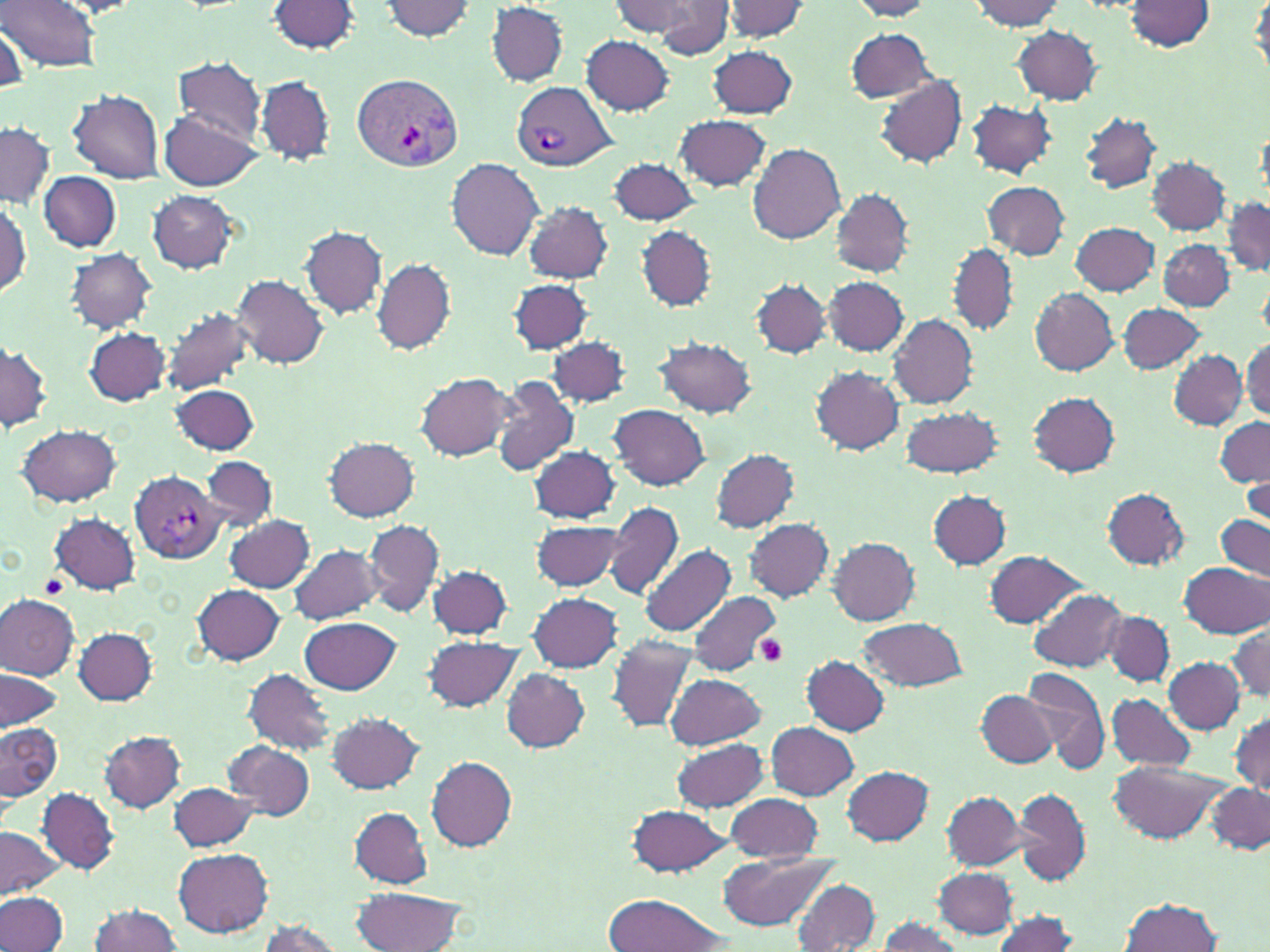

Approximate bounding boxes as (x1, y1, x2, y2) in pixels. Platelet locations: (39, 575, 67, 599), (756, 633, 789, 666). Uninfected red blood cell locations: (1, 0, 101, 72), (849, 0, 934, 20), (378, 1, 477, 41), (610, 1, 702, 40), (653, 1, 733, 57), (722, 1, 811, 41), (970, 1, 1069, 30), (1124, 1, 1214, 51), (1247, 1, 1270, 74), (267, 2, 361, 55), (486, 4, 569, 86), (2, 23, 26, 91), (1011, 25, 1102, 104), (845, 29, 934, 100), (581, 35, 674, 114), (708, 45, 797, 118), (173, 58, 267, 143), (255, 75, 336, 166), (874, 75, 968, 169), (68, 87, 165, 183), (966, 98, 1057, 179), (159, 110, 260, 190), (1080, 113, 1164, 194), (675, 115, 772, 191), (0, 123, 53, 208), (746, 142, 847, 244), (1148, 156, 1229, 235), (447, 157, 545, 260), (608, 158, 701, 226), (39, 171, 122, 252), (981, 180, 1069, 260), (832, 188, 914, 276), (145, 190, 244, 274), (0, 196, 31, 298), (1222, 196, 1270, 276), (523, 201, 613, 283), (1071, 221, 1161, 295), (301, 225, 385, 319), (637, 227, 717, 310), (1160, 239, 1233, 309), (947, 244, 1018, 334), (66, 248, 157, 333), (371, 259, 456, 354), (233, 275, 328, 368), (823, 275, 909, 356), (508, 279, 593, 355), (752, 279, 830, 358), (1029, 287, 1119, 375), (1117, 303, 1207, 374), (160, 308, 257, 396), (888, 314, 978, 406), (85, 327, 170, 405), (549, 335, 631, 406), (0, 337, 52, 433), (653, 337, 758, 419), (1242, 338, 1270, 421), (1168, 350, 1247, 429), (810, 366, 905, 455), (415, 372, 513, 460), (488, 374, 577, 477), (170, 384, 261, 456), (1029, 391, 1120, 477), (609, 405, 711, 491), (897, 405, 1003, 478), (1214, 416, 1269, 488), (16, 424, 122, 508), (325, 438, 419, 520), (528, 445, 621, 523), (710, 447, 798, 532), (201, 456, 277, 530), (1244, 471, 1270, 534), (1102, 487, 1190, 570), (929, 491, 1012, 569), (603, 500, 685, 601), (50, 512, 140, 593), (1216, 513, 1269, 581), (225, 515, 316, 593), (745, 518, 833, 601), (363, 519, 445, 619), (531, 520, 625, 593), (830, 537, 919, 625), (642, 543, 736, 639), (288, 544, 380, 626), (984, 550, 1086, 627), (1180, 561, 1270, 639), (428, 565, 513, 639), (192, 584, 285, 664), (1027, 588, 1129, 674), (528, 592, 623, 672), (688, 592, 781, 677), (0, 594, 81, 680), (1102, 610, 1175, 686), (300, 616, 400, 696), (858, 619, 969, 690), (1228, 622, 1269, 704), (74, 628, 158, 704), (424, 635, 524, 712), (607, 635, 699, 732), (803, 656, 890, 736), (1164, 657, 1243, 734), (1021, 667, 1109, 770), (0, 668, 64, 732), (243, 668, 337, 754), (501, 669, 589, 753), (664, 673, 765, 750), (975, 688, 1055, 768), (1105, 692, 1197, 771), (1230, 710, 1270, 796), (327, 713, 424, 794), (766, 722, 859, 800), (1, 723, 62, 804), (99, 731, 186, 812), (673, 736, 768, 813), (224, 740, 316, 820), (427, 756, 518, 851), (1108, 758, 1231, 845), (841, 767, 933, 844), (168, 782, 259, 852), (1206, 783, 1269, 853), (1012, 785, 1093, 887), (39, 788, 118, 873), (943, 791, 1026, 870), (723, 793, 824, 863), (627, 804, 735, 878), (349, 807, 433, 889), (0, 826, 65, 900), (173, 847, 272, 937), (718, 851, 836, 931), (934, 867, 1018, 937), (789, 878, 881, 951), (350, 886, 470, 952), (0, 892, 68, 952), (603, 895, 731, 952), (1121, 897, 1223, 952), (89, 902, 184, 952), (989, 913, 1079, 951), (876, 917, 966, 952), (255, 920, 345, 952). Plasmodium vivax-infected red blood cell locations: (350, 73, 462, 171), (513, 82, 614, 171), (129, 470, 226, 565). Slide-level diagnosis: Plasmodium vivax. Thin blood smear. May-Grünwald-Giemsa-stained preparation. Single field of view. Image is 1270×952 pixels. Light microscopy. Captured at 1000x magnification.